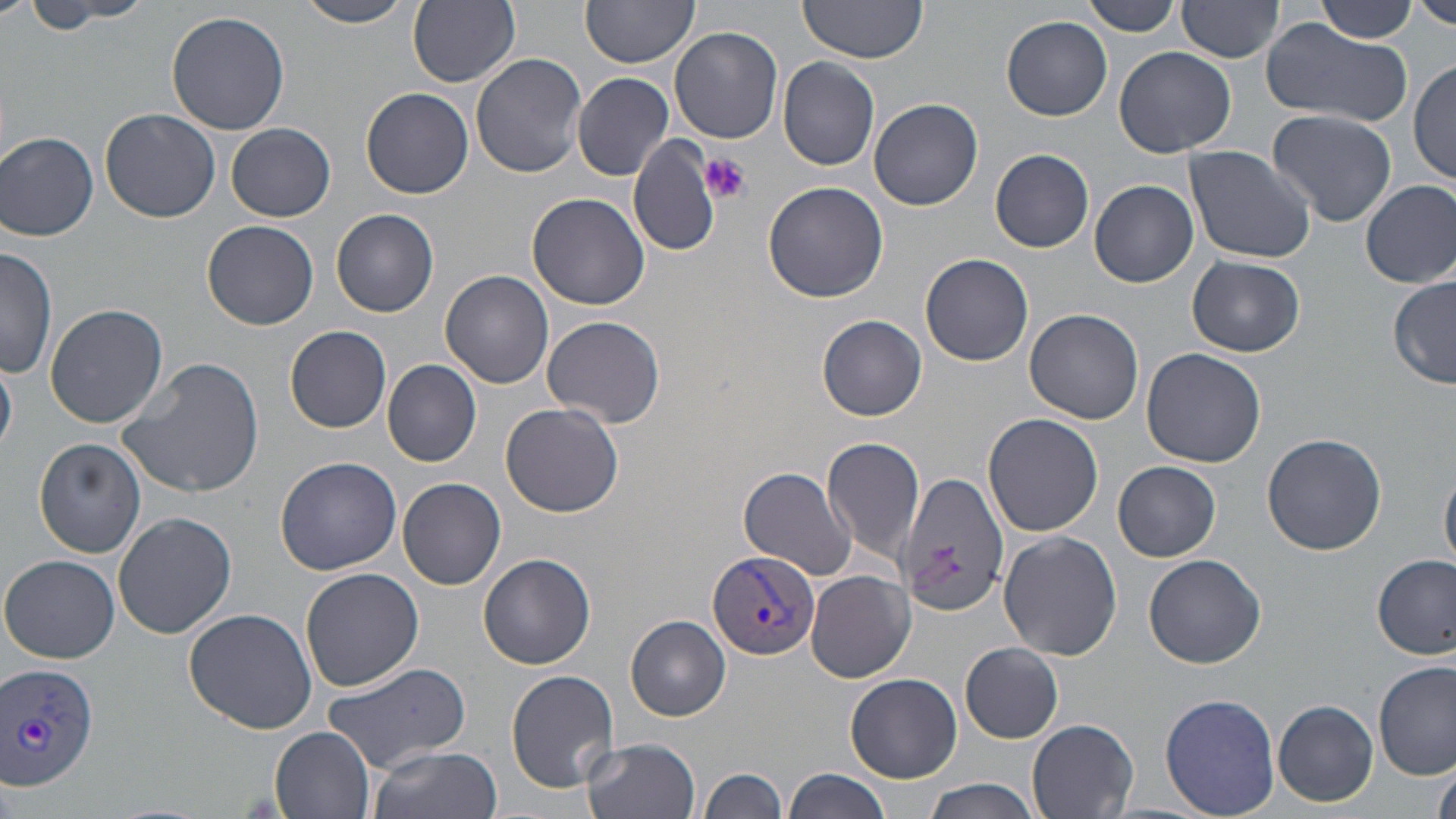
Approximate bounding boxes as (x1,y1)-(x2,y2) corner pairs in pixels. Plasmodium vivax-infected red blood cell locations: (708,550)-(820,662), (0,662)-(99,792). Platelet locations: (702,153)-(751,204). Uninfected red blood cell locations: (17,0)-(143,29), (294,0)-(417,26), (798,0)-(932,69), (1082,0)-(1182,37), (1416,0)-(1456,31), (408,1)-(520,88), (582,1)-(699,69), (1177,2)-(1284,65), (1315,2)-(1419,44), (165,10)-(291,135), (1002,16)-(1112,121), (1258,17)-(1415,127), (670,26)-(784,144), (1113,46)-(1238,159), (470,53)-(586,178), (777,57)-(880,171), (1410,58)-(1456,187), (571,73)-(675,181), (360,87)-(474,199), (869,99)-(983,210), (99,107)-(220,223), (1267,109)-(1396,226), (226,124)-(335,222), (2,130)-(99,241), (630,135)-(718,258), (1184,144)-(1316,263), (991,148)-(1094,253), (762,179)-(890,302), (1088,179)-(1200,287), (1360,180)-(1456,289), (527,192)-(652,311), (332,209)-(440,318), (202,220)-(319,330), (0,246)-(58,380), (921,253)-(1034,366), (1186,256)-(1305,357), (441,269)-(554,388), (1389,274)-(1455,389), (43,303)-(167,429), (1024,308)-(1144,424), (817,314)-(925,420), (541,315)-(667,428), (285,325)-(393,433), (1140,348)-(1266,468), (0,352)-(19,455), (119,356)-(265,498), (383,359)-(481,467), (501,402)-(623,517), (982,412)-(1104,537), (1262,432)-(1386,555), (822,435)-(928,567), (33,437)-(146,558), (273,457)-(402,574), (1113,460)-(1221,561), (1440,462)-(1456,569), (738,466)-(859,579), (898,473)-(1013,620), (398,476)-(506,590), (113,513)-(237,641), (999,532)-(1123,661), (1373,552)-(1454,659), (480,553)-(596,671), (1,554)-(121,663), (1143,554)-(1267,669), (301,566)-(424,692), (806,570)-(915,683), (183,608)-(318,735), (626,614)-(730,721), (960,642)-(1064,743), (1374,661)-(1454,781), (321,662)-(472,772), (506,669)-(620,791), (846,673)-(962,783), (1160,693)-(1281,817), (1273,699)-(1378,806), (1027,719)-(1140,819), (271,726)-(376,819), (583,736)-(702,819), (366,746)-(504,819), (1433,762)-(1456,819), (700,766)-(786,819), (784,767)-(896,819), (919,778)-(1042,819). Slide-level diagnosis: Plasmodium vivax. Image is 1456×819 pixels. Single field of view. Thin blood film. Light microscopy. May-Grünwald-Giemsa-stained preparation. 1000x magnification.